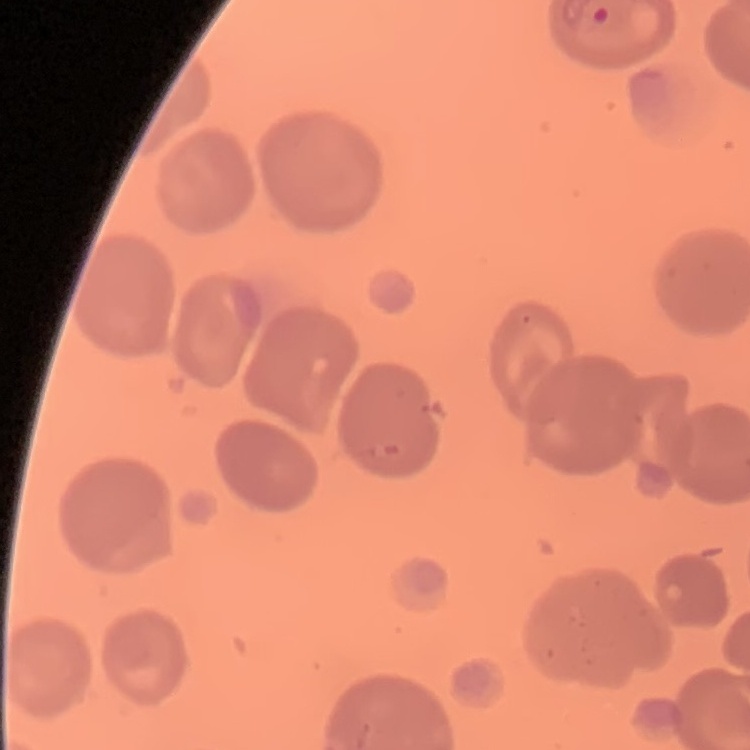

Summary:
  - Erythrocyte morphology: no rouleaux formation
  - Image type: square crop of a larger photomicrograph
  - Preparation: thin peripheral smear
  - Stain: Field's or Giemsa